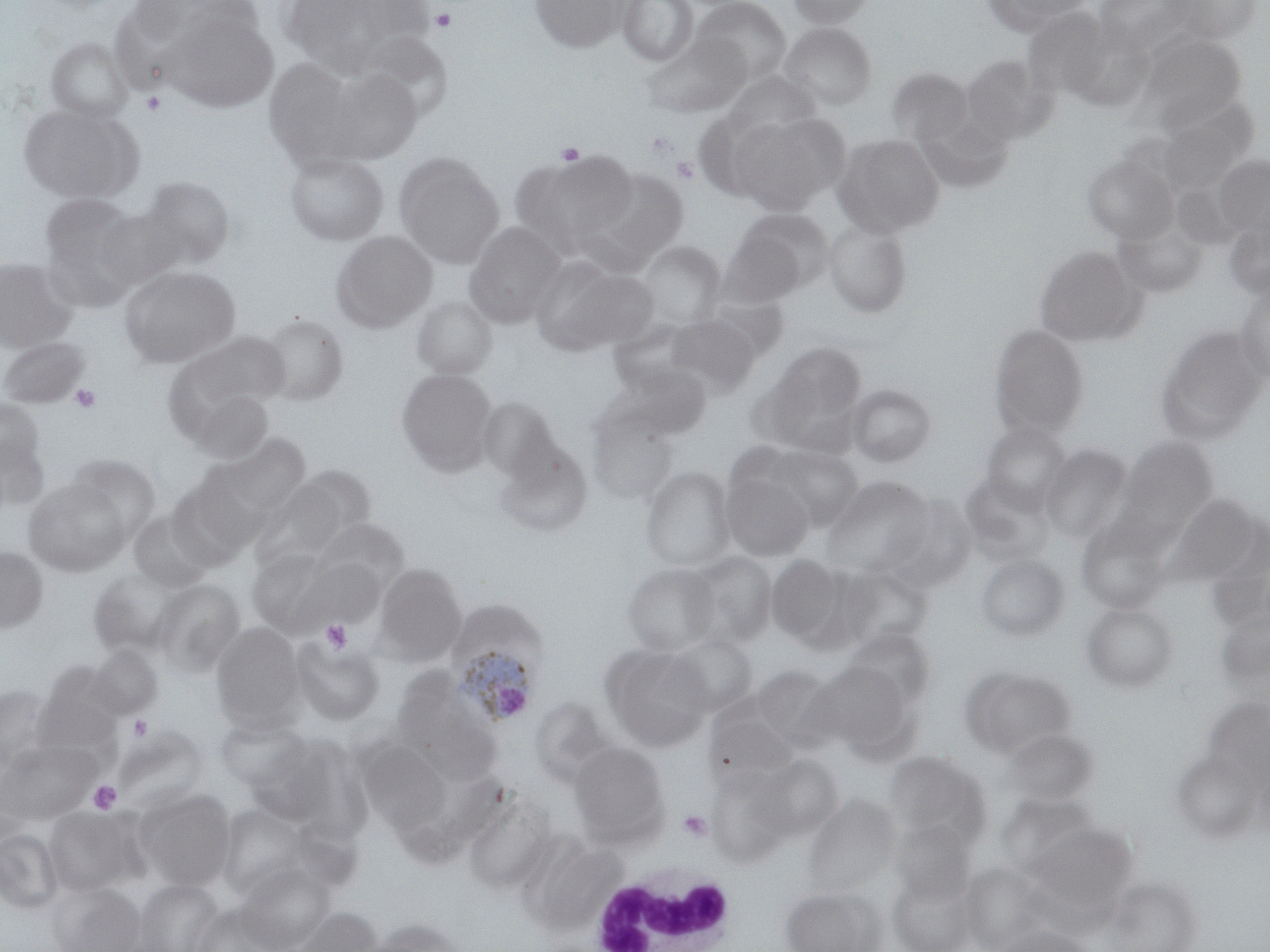
{
  "slide_level_diagnosis": "Plasmodium ovale",
  "magnification": "1000x",
  "preparation": "thin blood smear",
  "image_size": "1270×952 pixels",
  "plasmodium_ovale_infected_red_blood_cell_locations": "approximate bounding boxes as named x1/y1/x2/y2 corners in pixels: (x1=446, y1=628, x2=546, y2=729)",
  "stain": "May-Grünwald-Giemsa",
  "field_of_view": "one of a larger specimen",
  "modality": "light microscopy",
  "platelet_locations": "approximate bounding boxes as named x1/y1/x2/y2 corners in pixels: (x1=430, y1=6, x2=458, y2=33), (x1=141, y1=90, x2=166, y2=116), (x1=645, y1=131, x2=679, y2=162), (x1=556, y1=142, x2=585, y2=165), (x1=672, y1=157, x2=699, y2=183), (x1=69, y1=383, x2=101, y2=413), (x1=320, y1=619, x2=352, y2=654), (x1=128, y1=715, x2=152, y2=740), (x1=88, y1=780, x2=122, y2=814), (x1=678, y1=809, x2=713, y2=842)",
  "white_blood_cell_locations": "approximate bounding boxes as named x1/y1/x2/y2 corners in pixels: (x1=584, y1=863, x2=739, y2=950)",
  "uninfected_red_blood_cell_locations": "approximate bounding boxes as named x1/y1/x2/y2 corners in pixels: (x1=277, y1=0, x2=405, y2=76), (x1=529, y1=0, x2=628, y2=52), (x1=616, y1=0, x2=698, y2=67), (x1=693, y1=0, x2=792, y2=85), (x1=787, y1=0, x2=874, y2=29), (x1=983, y1=0, x2=1096, y2=35), (x1=1094, y1=0, x2=1192, y2=58), (x1=1165, y1=0, x2=1260, y2=43), (x1=164, y1=8, x2=279, y2=113), (x1=1023, y1=9, x2=1112, y2=100), (x1=780, y1=23, x2=877, y2=111), (x1=641, y1=33, x2=748, y2=119), (x1=1140, y1=35, x2=1245, y2=128), (x1=46, y1=37, x2=133, y2=123), (x1=960, y1=55, x2=1056, y2=145), (x1=263, y1=57, x2=361, y2=169), (x1=318, y1=67, x2=424, y2=164), (x1=887, y1=68, x2=971, y2=147), (x1=722, y1=73, x2=820, y2=143), (x1=20, y1=104, x2=139, y2=203), (x1=693, y1=109, x2=782, y2=201), (x1=915, y1=111, x2=1013, y2=193), (x1=730, y1=114, x2=838, y2=215), (x1=1157, y1=117, x2=1244, y2=194), (x1=834, y1=133, x2=944, y2=237), (x1=512, y1=150, x2=637, y2=257), (x1=1082, y1=151, x2=1176, y2=243), (x1=284, y1=152, x2=389, y2=246), (x1=394, y1=153, x2=504, y2=268), (x1=1214, y1=155, x2=1270, y2=237), (x1=581, y1=166, x2=691, y2=271), (x1=138, y1=176, x2=235, y2=269), (x1=1172, y1=182, x2=1243, y2=250), (x1=39, y1=193, x2=142, y2=291), (x1=94, y1=208, x2=181, y2=287), (x1=731, y1=209, x2=833, y2=294), (x1=823, y1=218, x2=912, y2=318), (x1=1224, y1=218, x2=1270, y2=298), (x1=1113, y1=219, x2=1206, y2=296), (x1=463, y1=221, x2=566, y2=328), (x1=331, y1=230, x2=437, y2=333), (x1=717, y1=232, x2=806, y2=307), (x1=638, y1=241, x2=725, y2=325), (x1=1035, y1=246, x2=1142, y2=346), (x1=530, y1=256, x2=640, y2=356), (x1=0, y1=257, x2=78, y2=352), (x1=119, y1=265, x2=240, y2=367), (x1=1234, y1=281, x2=1270, y2=384), (x1=412, y1=296, x2=497, y2=380), (x1=259, y1=314, x2=349, y2=406), (x1=665, y1=314, x2=760, y2=399), (x1=988, y1=324, x2=1089, y2=439), (x1=1155, y1=325, x2=1268, y2=446), (x1=172, y1=331, x2=290, y2=421), (x1=0, y1=336, x2=90, y2=408), (x1=758, y1=342, x2=868, y2=451), (x1=606, y1=364, x2=711, y2=442), (x1=397, y1=369, x2=497, y2=474), (x1=847, y1=383, x2=937, y2=467), (x1=184, y1=386, x2=274, y2=465), (x1=0, y1=397, x2=46, y2=480), (x1=477, y1=398, x2=559, y2=482), (x1=586, y1=404, x2=679, y2=504), (x1=980, y1=422, x2=1069, y2=511), (x1=0, y1=429, x2=50, y2=513), (x1=217, y1=434, x2=310, y2=516), (x1=1117, y1=435, x2=1218, y2=536), (x1=494, y1=439, x2=591, y2=537), (x1=1040, y1=443, x2=1132, y2=544), (x1=761, y1=444, x2=863, y2=531), (x1=65, y1=454, x2=161, y2=541), (x1=770, y1=455, x2=919, y2=559), (x1=641, y1=466, x2=735, y2=571), (x1=283, y1=467, x2=375, y2=547), (x1=720, y1=470, x2=814, y2=561), (x1=959, y1=474, x2=1054, y2=566), (x1=823, y1=475, x2=934, y2=578), (x1=25, y1=478, x2=130, y2=576), (x1=250, y1=481, x2=350, y2=572), (x1=883, y1=494, x2=977, y2=593), (x1=1168, y1=494, x2=1260, y2=582), (x1=127, y1=510, x2=214, y2=591), (x1=1075, y1=513, x2=1173, y2=613), (x1=311, y1=519, x2=409, y2=595), (x1=0, y1=545, x2=48, y2=633), (x1=246, y1=549, x2=340, y2=636), (x1=683, y1=551, x2=777, y2=648), (x1=766, y1=554, x2=846, y2=645), (x1=975, y1=554, x2=1070, y2=641), (x1=288, y1=557, x2=387, y2=633), (x1=374, y1=563, x2=465, y2=665), (x1=623, y1=563, x2=720, y2=655), (x1=830, y1=563, x2=933, y2=651), (x1=87, y1=566, x2=188, y2=657), (x1=150, y1=578, x2=244, y2=674), (x1=1082, y1=603, x2=1177, y2=692), (x1=1215, y1=606, x2=1270, y2=695), (x1=211, y1=621, x2=305, y2=730), (x1=841, y1=627, x2=935, y2=712), (x1=668, y1=634, x2=758, y2=716), (x1=292, y1=640, x2=384, y2=726), (x1=602, y1=644, x2=714, y2=750), (x1=90, y1=645, x2=162, y2=718), (x1=810, y1=662, x2=915, y2=753), (x1=33, y1=664, x2=125, y2=754), (x1=748, y1=666, x2=835, y2=747), (x1=960, y1=666, x2=1075, y2=759), (x1=390, y1=676, x2=501, y2=783), (x1=0, y1=685, x2=56, y2=774), (x1=529, y1=696, x2=613, y2=784), (x1=1200, y1=697, x2=1270, y2=791), (x1=706, y1=712, x2=797, y2=783), (x1=215, y1=716, x2=310, y2=791), (x1=114, y1=725, x2=208, y2=813), (x1=1001, y1=729, x2=1099, y2=806), (x1=244, y1=737, x2=356, y2=832), (x1=0, y1=738, x2=99, y2=825), (x1=358, y1=739, x2=453, y2=832), (x1=569, y1=742, x2=669, y2=844), (x1=1171, y1=749, x2=1263, y2=842), (x1=884, y1=750, x2=991, y2=847), (x1=753, y1=754, x2=843, y2=842), (x1=708, y1=768, x2=796, y2=865), (x1=134, y1=788, x2=236, y2=890), (x1=462, y1=792, x2=556, y2=894), (x1=802, y1=793, x2=900, y2=898), (x1=997, y1=793, x2=1097, y2=875), (x1=217, y1=803, x2=319, y2=898), (x1=44, y1=806, x2=144, y2=896), (x1=889, y1=820, x2=976, y2=905), (x1=1022, y1=821, x2=1136, y2=915), (x1=0, y1=827, x2=64, y2=913), (x1=520, y1=835, x2=625, y2=935), (x1=960, y1=862, x2=1053, y2=951), (x1=236, y1=863, x2=334, y2=951), (x1=888, y1=871, x2=978, y2=952), (x1=133, y1=878, x2=223, y2=952), (x1=1102, y1=878, x2=1200, y2=952), (x1=49, y1=881, x2=145, y2=952), (x1=781, y1=885, x2=886, y2=952), (x1=191, y1=903, x2=282, y2=952), (x1=289, y1=906, x2=383, y2=952), (x1=365, y1=917, x2=468, y2=952), (x1=993, y1=924, x2=1096, y2=952)"
}